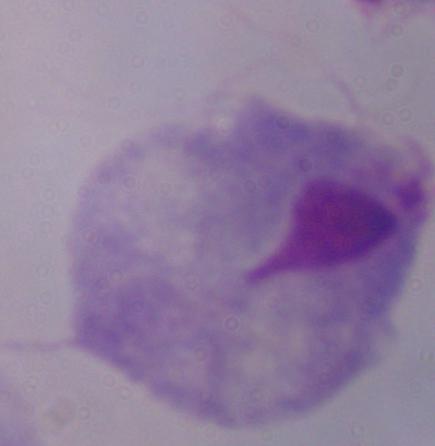

A trichomonad is shown. Micrograph. 1000x magnification.